Describe the morphology of the erythrocytes.
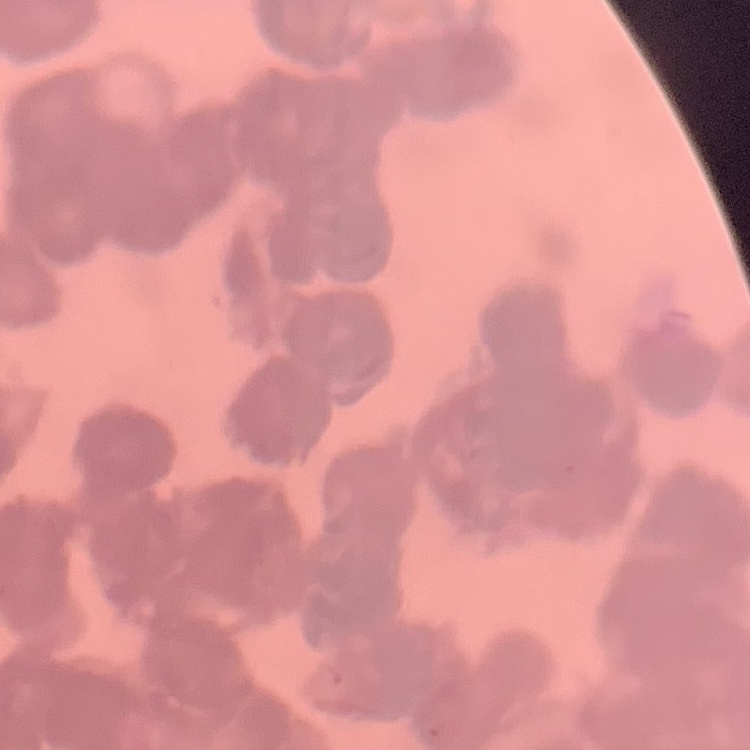
Rouleaux formation.

Summary:
  - Stain: Field's or Giemsa
  - Image type: square crop of a larger photomicrograph
  - Preparation: thin peripheral smear